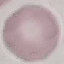

Summary:
  - Malaria status: uninfected
  - Image type: automatically extracted cell patch, resized to 64 × 64 pixels
  - Stain: Giemsa
  - Capture: smartphone camera at the microscope eyepiece
  - Preparation: thin blood film